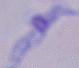
Summary:
  - Identification: trypanosome
  - Modality: micrograph
  - Magnification: 1000x